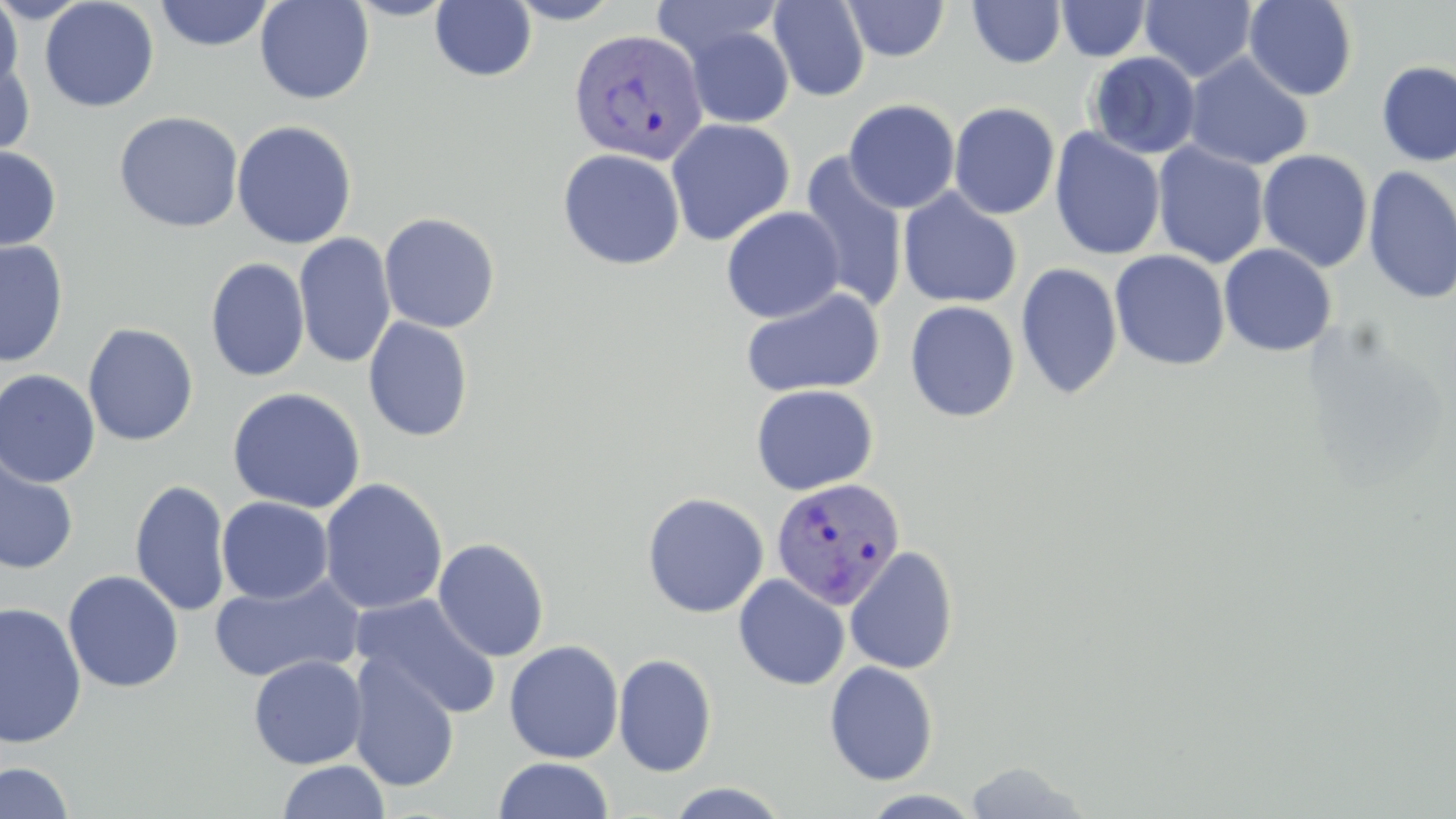

Summary:
  - Coordinate format: approximate bounding boxes as (x1,y1)-(x2,y2) corner pairs in pixels
  - Uninfected red blood cell locations: (39,0)-(160,112), (254,0)-(375,105), (345,0)-(457,21), (430,0)-(537,82), (505,0)-(623,24), (652,0)-(782,65), (768,0)-(870,102), (843,0)-(950,62), (1140,0)-(1257,83), (1244,0)-(1358,101), (0,1)-(25,93), (154,1)-(275,51), (967,1)-(1066,68), (1056,1)-(1151,61), (686,26)-(794,128), (1087,51)-(1202,159), (0,52)-(36,162), (1184,53)-(1312,170), (1375,61)-(1456,167), (843,98)-(961,213), (948,101)-(1060,220), (113,111)-(244,233), (666,118)-(796,246), (231,119)-(358,250), (691,126)-(825,318), (1048,128)-(1166,262), (1152,142)-(1270,268), (0,146)-(61,251), (557,148)-(685,270), (1257,149)-(1373,273), (798,153)-(909,314), (1363,165)-(1456,305), (898,188)-(1023,309), (721,206)-(845,323), (379,211)-(501,333), (294,233)-(396,369), (0,240)-(69,368), (1219,243)-(1337,357), (1110,250)-(1231,371), (205,257)-(310,382), (1015,262)-(1123,400), (740,286)-(885,399), (904,300)-(1020,422), (363,315)-(474,442), (82,323)-(199,446), (0,369)-(101,488), (750,384)-(879,496), (226,387)-(366,514), (0,450)-(79,575), (319,477)-(448,616), (130,479)-(232,617), (641,492)-(769,619), (216,496)-(334,604), (432,537)-(550,662), (844,546)-(959,675), (63,570)-(184,693), (733,573)-(851,690), (207,574)-(366,685), (352,594)-(502,719), (0,601)-(88,749), (504,640)-(624,764), (347,653)-(460,792), (613,653)-(717,777), (248,655)-(368,770), (823,660)-(939,785), (492,757)-(615,818), (276,760)-(391,819), (963,760)-(1091,818), (0,761)-(75,819), (664,782)-(791,818), (863,790)-(984,819)
  - Plasmodium vivax-infected red blood cell locations: (568,28)-(709,165), (770,477)-(907,609)
  - Slide-level diagnosis: Plasmodium vivax
  - Preparation: thin blood film
  - Modality: optical microscopy
  - Magnification: 1000x
  - Stain: May-Grünwald-Giemsa
  - Field of view: single
  - Image size: 1456×819 pixels